State the blood parasite species.
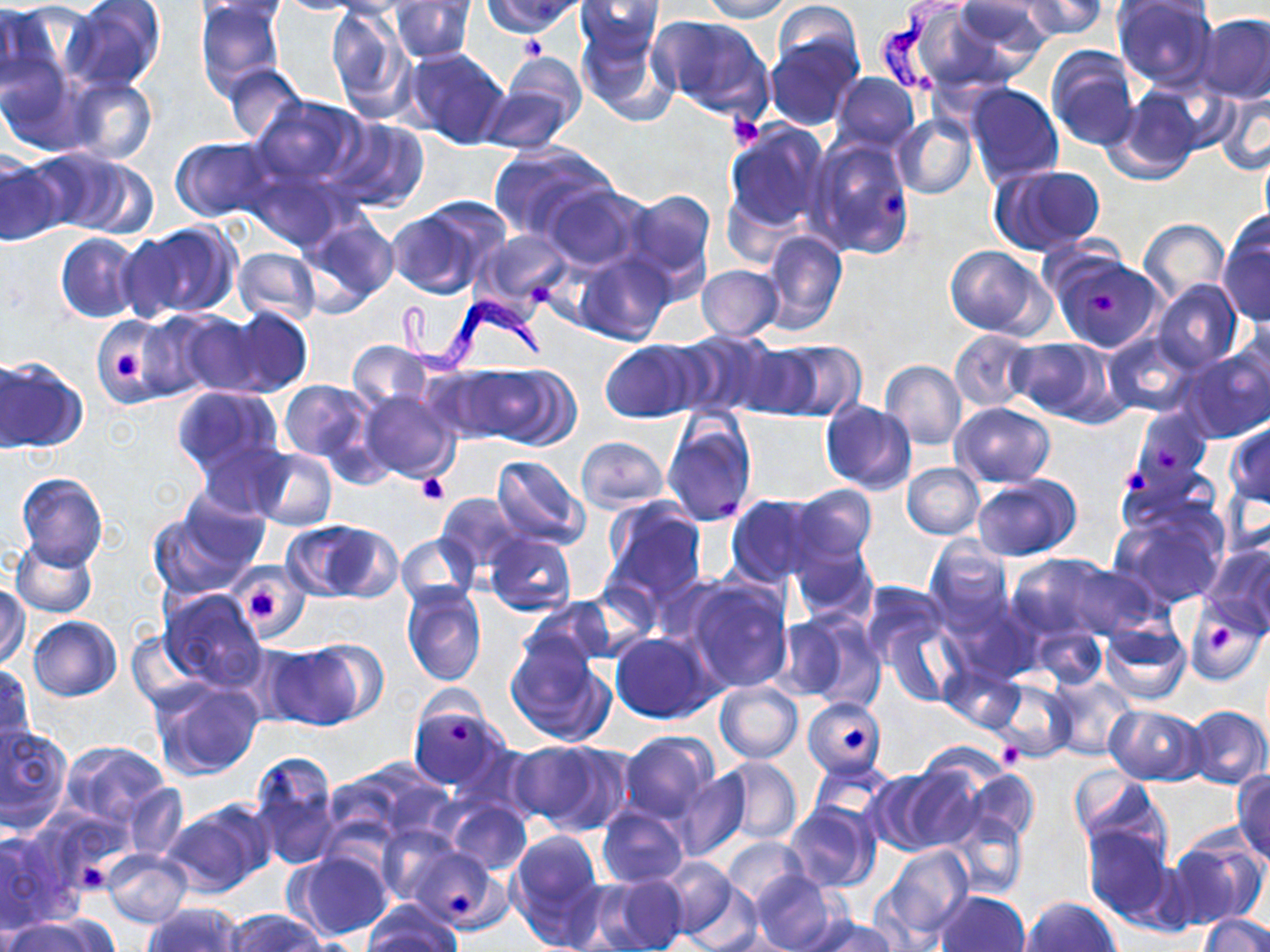

Trypanosoma brucei.

image size = 1270×952 pixels
magnification = 1000x
uninfected red blood cell locations = approximate bounding boxes as named x1/y1/x2/y2 corners in pixels: (x1=63, y1=0, x2=165, y2=93), (x1=195, y1=0, x2=287, y2=98), (x1=196, y1=0, x2=293, y2=21), (x1=483, y1=0, x2=585, y2=36), (x1=698, y1=0, x2=795, y2=23), (x1=949, y1=0, x2=1048, y2=70), (x1=970, y1=0, x2=1087, y2=47), (x1=1018, y1=0, x2=1108, y2=39), (x1=1113, y1=0, x2=1217, y2=88), (x1=1114, y1=0, x2=1217, y2=24), (x1=272, y1=1, x2=369, y2=15), (x1=576, y1=1, x2=665, y2=57), (x1=388, y1=2, x2=476, y2=63), (x1=770, y1=3, x2=866, y2=86), (x1=0, y1=4, x2=72, y2=101), (x1=910, y1=4, x2=1022, y2=90), (x1=327, y1=5, x2=411, y2=121), (x1=1196, y1=13, x2=1270, y2=103), (x1=651, y1=14, x2=774, y2=120), (x1=576, y1=19, x2=679, y2=127), (x1=766, y1=35, x2=860, y2=130), (x1=1046, y1=46, x2=1139, y2=151), (x1=402, y1=48, x2=511, y2=150), (x1=502, y1=53, x2=587, y2=134), (x1=2, y1=57, x2=84, y2=155), (x1=222, y1=63, x2=307, y2=144), (x1=832, y1=72, x2=918, y2=151), (x1=62, y1=75, x2=157, y2=165), (x1=477, y1=81, x2=579, y2=153), (x1=964, y1=82, x2=1063, y2=188), (x1=1108, y1=87, x2=1202, y2=184), (x1=1215, y1=87, x2=1270, y2=176), (x1=249, y1=95, x2=365, y2=191), (x1=893, y1=112, x2=978, y2=200), (x1=324, y1=117, x2=431, y2=214), (x1=725, y1=121, x2=831, y2=234), (x1=171, y1=136, x2=273, y2=223), (x1=808, y1=136, x2=915, y2=259), (x1=487, y1=143, x2=614, y2=243), (x1=31, y1=148, x2=154, y2=238), (x1=0, y1=150, x2=67, y2=245), (x1=991, y1=164, x2=1104, y2=255), (x1=247, y1=168, x2=344, y2=251), (x1=542, y1=185, x2=644, y2=272), (x1=622, y1=189, x2=716, y2=287), (x1=398, y1=198, x2=509, y2=297), (x1=297, y1=214, x2=400, y2=312), (x1=1218, y1=216, x2=1270, y2=325), (x1=1139, y1=218, x2=1230, y2=304), (x1=125, y1=222, x2=240, y2=320), (x1=759, y1=228, x2=847, y2=337), (x1=476, y1=229, x2=573, y2=309), (x1=55, y1=232, x2=141, y2=324), (x1=945, y1=245, x2=1049, y2=338), (x1=232, y1=248, x2=320, y2=325), (x1=576, y1=250, x2=674, y2=345), (x1=1052, y1=251, x2=1168, y2=378), (x1=697, y1=265, x2=783, y2=341), (x1=1149, y1=281, x2=1242, y2=373), (x1=225, y1=305, x2=312, y2=397), (x1=159, y1=310, x2=262, y2=397), (x1=132, y1=315, x2=222, y2=400), (x1=93, y1=316, x2=171, y2=400), (x1=1230, y1=321, x2=1270, y2=416), (x1=950, y1=329, x2=1037, y2=412), (x1=672, y1=330, x2=780, y2=417), (x1=1103, y1=330, x2=1202, y2=418), (x1=1007, y1=338, x2=1112, y2=421), (x1=598, y1=339, x2=705, y2=421), (x1=346, y1=341, x2=431, y2=412), (x1=762, y1=341, x2=867, y2=421), (x1=1182, y1=344, x2=1270, y2=442), (x1=1, y1=354, x2=30, y2=455), (x1=1, y1=356, x2=87, y2=453), (x1=880, y1=360, x2=966, y2=449), (x1=462, y1=364, x2=579, y2=450), (x1=279, y1=379, x2=370, y2=463), (x1=173, y1=386, x2=285, y2=478), (x1=357, y1=389, x2=461, y2=484), (x1=820, y1=401, x2=917, y2=495), (x1=951, y1=402, x2=1055, y2=487), (x1=1130, y1=409, x2=1212, y2=495), (x1=661, y1=413, x2=756, y2=525), (x1=1225, y1=422, x2=1270, y2=510), (x1=575, y1=436, x2=669, y2=512), (x1=194, y1=441, x2=293, y2=519), (x1=251, y1=448, x2=337, y2=530), (x1=491, y1=455, x2=590, y2=550), (x1=901, y1=463, x2=984, y2=538), (x1=14, y1=473, x2=108, y2=568), (x1=972, y1=474, x2=1079, y2=561), (x1=790, y1=484, x2=877, y2=568), (x1=178, y1=490, x2=272, y2=575), (x1=437, y1=493, x2=523, y2=574), (x1=726, y1=494, x2=824, y2=585), (x1=603, y1=501, x2=707, y2=606), (x1=1111, y1=507, x2=1228, y2=608), (x1=147, y1=509, x2=258, y2=599), (x1=285, y1=519, x2=400, y2=602), (x1=396, y1=534, x2=479, y2=608), (x1=484, y1=535, x2=576, y2=617), (x1=10, y1=537, x2=98, y2=618), (x1=790, y1=537, x2=876, y2=621), (x1=925, y1=538, x2=1013, y2=634), (x1=1201, y1=543, x2=1270, y2=635), (x1=1007, y1=552, x2=1125, y2=640), (x1=1055, y1=559, x2=1159, y2=638), (x1=230, y1=565, x2=308, y2=639), (x1=685, y1=578, x2=793, y2=693), (x1=860, y1=581, x2=947, y2=663), (x1=0, y1=582, x2=30, y2=668), (x1=402, y1=584, x2=488, y2=686), (x1=159, y1=589, x2=265, y2=689), (x1=519, y1=599, x2=616, y2=678), (x1=1186, y1=603, x2=1264, y2=685), (x1=769, y1=613, x2=852, y2=702), (x1=796, y1=614, x2=887, y2=712), (x1=28, y1=616, x2=121, y2=701), (x1=882, y1=621, x2=963, y2=706), (x1=1099, y1=621, x2=1191, y2=705), (x1=1034, y1=628, x2=1106, y2=687), (x1=129, y1=630, x2=211, y2=714), (x1=611, y1=633, x2=716, y2=723), (x1=505, y1=636, x2=615, y2=746), (x1=265, y1=642, x2=370, y2=731), (x1=1, y1=663, x2=33, y2=758), (x1=941, y1=665, x2=1022, y2=732), (x1=1046, y1=674, x2=1138, y2=763), (x1=150, y1=678, x2=263, y2=780), (x1=990, y1=678, x2=1073, y2=761), (x1=713, y1=682, x2=802, y2=762), (x1=803, y1=696, x2=887, y2=780), (x1=408, y1=702, x2=508, y2=791), (x1=1106, y1=704, x2=1206, y2=785), (x1=1185, y1=706, x2=1269, y2=789), (x1=1, y1=723, x2=73, y2=831), (x1=619, y1=730, x2=717, y2=822), (x1=61, y1=741, x2=171, y2=827), (x1=509, y1=742, x2=617, y2=832), (x1=250, y1=751, x2=342, y2=871), (x1=716, y1=757, x2=802, y2=844), (x1=809, y1=759, x2=899, y2=832), (x1=322, y1=760, x2=447, y2=846), (x1=897, y1=762, x2=989, y2=852), (x1=668, y1=767, x2=750, y2=862), (x1=1069, y1=768, x2=1166, y2=858), (x1=865, y1=769, x2=957, y2=855), (x1=966, y1=770, x2=1039, y2=846), (x1=1232, y1=770, x2=1270, y2=866), (x1=121, y1=785, x2=187, y2=862), (x1=444, y1=799, x2=532, y2=876), (x1=162, y1=802, x2=271, y2=898), (x1=784, y1=802, x2=880, y2=891), (x1=596, y1=806, x2=690, y2=888), (x1=947, y1=815, x2=1027, y2=900), (x1=377, y1=823, x2=463, y2=906), (x1=1082, y1=824, x2=1178, y2=928), (x1=0, y1=828, x2=79, y2=934), (x1=507, y1=829, x2=605, y2=946), (x1=1163, y1=835, x2=1268, y2=930), (x1=722, y1=838, x2=807, y2=907), (x1=878, y1=845, x2=974, y2=942), (x1=407, y1=846, x2=508, y2=931), (x1=101, y1=849, x2=193, y2=927), (x1=287, y1=850, x2=395, y2=941), (x1=659, y1=856, x2=741, y2=943), (x1=750, y1=870, x2=843, y2=952), (x1=594, y1=874, x2=690, y2=952), (x1=936, y1=890, x2=1028, y2=952), (x1=1022, y1=896, x2=1119, y2=952), (x1=363, y1=901, x2=460, y2=951), (x1=144, y1=903, x2=242, y2=951), (x1=224, y1=909, x2=323, y2=952), (x1=1199, y1=915, x2=1270, y2=952), (x1=3, y1=916, x2=112, y2=952), (x1=801, y1=916, x2=899, y2=952)
preparation = thin blood smear
modality = light microscopy
platelet locations = approximate bounding boxes as named x1/y1/x2/y2 corners in pixels: (x1=518, y1=35, x2=548, y2=63), (x1=726, y1=115, x2=763, y2=150), (x1=882, y1=190, x2=907, y2=217), (x1=528, y1=281, x2=552, y2=304), (x1=1089, y1=290, x2=1116, y2=313), (x1=116, y1=351, x2=139, y2=379), (x1=1156, y1=446, x2=1180, y2=471), (x1=1119, y1=465, x2=1151, y2=497), (x1=417, y1=473, x2=448, y2=504), (x1=717, y1=496, x2=738, y2=517), (x1=249, y1=586, x2=278, y2=623), (x1=1208, y1=626, x2=1233, y2=654), (x1=449, y1=721, x2=473, y2=746), (x1=843, y1=727, x2=865, y2=749), (x1=995, y1=741, x2=1025, y2=768), (x1=81, y1=863, x2=104, y2=890), (x1=450, y1=893, x2=472, y2=915)
stain = May-Grünwald-Giemsa
field of view = single
Trypanosoma brucei locations = approximate bounding boxes as named x1/y1/x2/y2 corners in pixels: (x1=872, y1=0, x2=967, y2=93), (x1=392, y1=290, x2=541, y2=374)